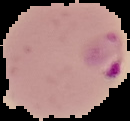
Summary:
  - Preparation: thin blood smear
  - Image type: segmented cell region with the area outside set to black
  - Image size: 130×121 pixels
  - Malaria status: parasitized